Outline platelets.
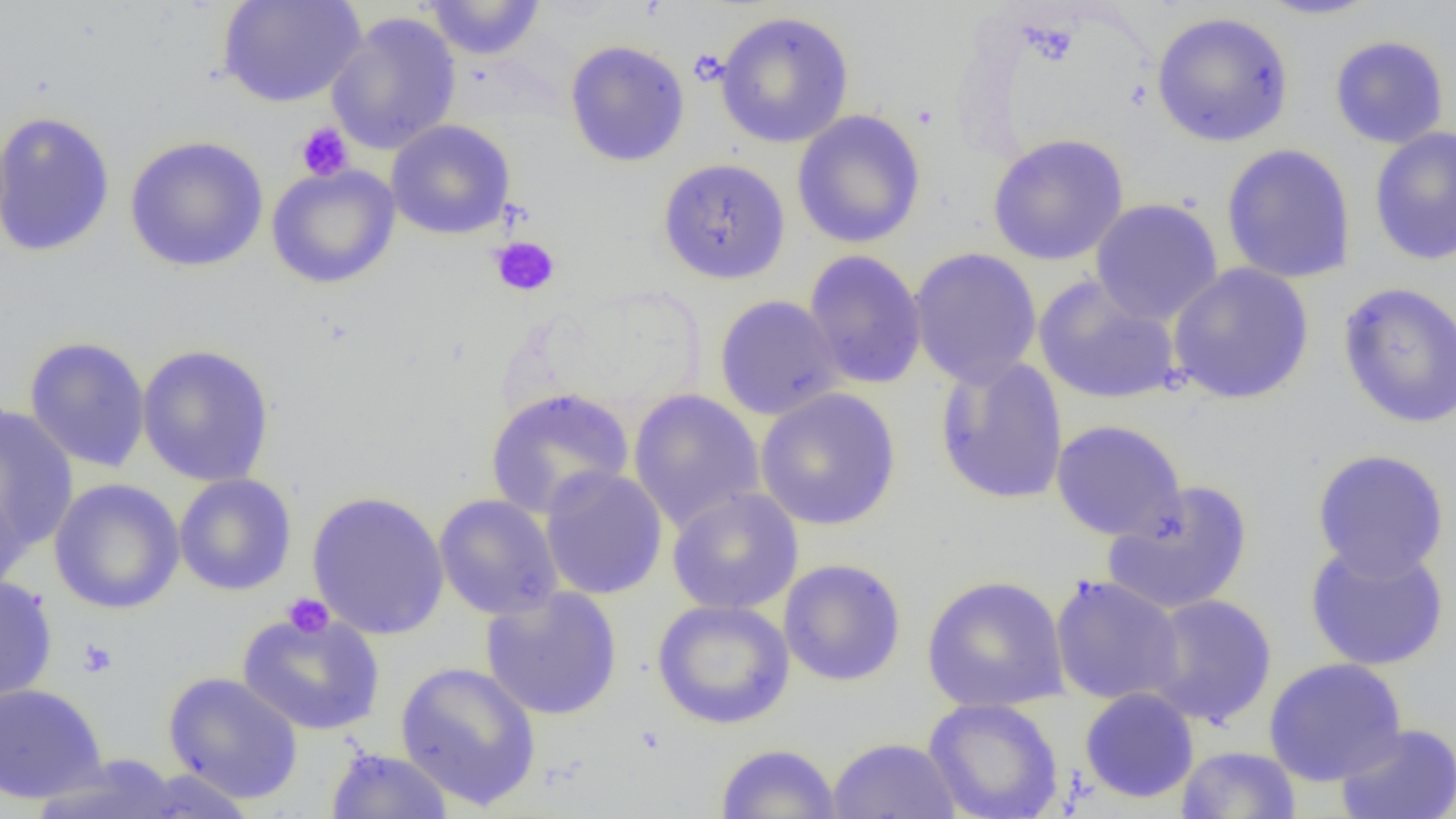

Approximate bounding boxes as (x1, y1, x2, y2) in pixels.
Platelets: (295, 122, 353, 181), (489, 236, 560, 296), (282, 593, 334, 638), (77, 637, 118, 678).

Summary:
  - Uninfected red blood cell locations: (218, 0, 366, 108), (423, 0, 546, 60), (1252, 0, 1386, 21), (714, 11, 855, 149), (1150, 11, 1295, 148), (326, 13, 462, 155), (1329, 34, 1449, 149), (565, 40, 690, 167), (791, 109, 927, 248), (0, 110, 116, 260), (385, 119, 516, 240), (1369, 126, 1456, 266), (988, 133, 1129, 266), (124, 135, 269, 273), (1221, 143, 1356, 284), (658, 157, 791, 285), (266, 163, 401, 289), (1089, 198, 1224, 325), (909, 247, 1042, 389), (804, 249, 927, 390), (1167, 262, 1315, 404), (1033, 275, 1182, 406), (1337, 281, 1456, 430), (713, 294, 845, 421), (23, 335, 151, 473), (136, 343, 275, 487), (934, 356, 1069, 505), (484, 387, 634, 520), (628, 388, 765, 532), (755, 388, 901, 530), (0, 405, 78, 553), (1050, 419, 1187, 542), (1312, 448, 1450, 580), (540, 467, 668, 601), (174, 473, 297, 596), (48, 478, 185, 614), (1102, 480, 1254, 616), (0, 481, 31, 600), (667, 487, 804, 615), (306, 489, 450, 640), (434, 493, 563, 620), (1304, 540, 1450, 672), (778, 558, 907, 687), (0, 574, 57, 706), (920, 574, 1070, 713), (1050, 574, 1185, 706), (480, 586, 623, 721), (1143, 593, 1278, 728), (651, 599, 795, 729), (237, 609, 385, 736), (1263, 657, 1407, 786), (395, 660, 542, 810), (162, 671, 304, 804), (0, 683, 107, 804), (1079, 687, 1199, 804), (923, 697, 1064, 819), (1335, 722, 1455, 819), (827, 736, 961, 819), (715, 742, 842, 819), (325, 746, 454, 818), (1176, 746, 1302, 818), (30, 754, 188, 819), (129, 770, 260, 819)
  - Slide-level diagnosis: negative for blood parasites
  - Image size: 1456×819 pixels
  - Modality: optical microscopy
  - Field of view: one of a larger specimen
  - Preparation: thin blood smear
  - Magnification: 1000x